Comment on the morphology of the erythrocytes.
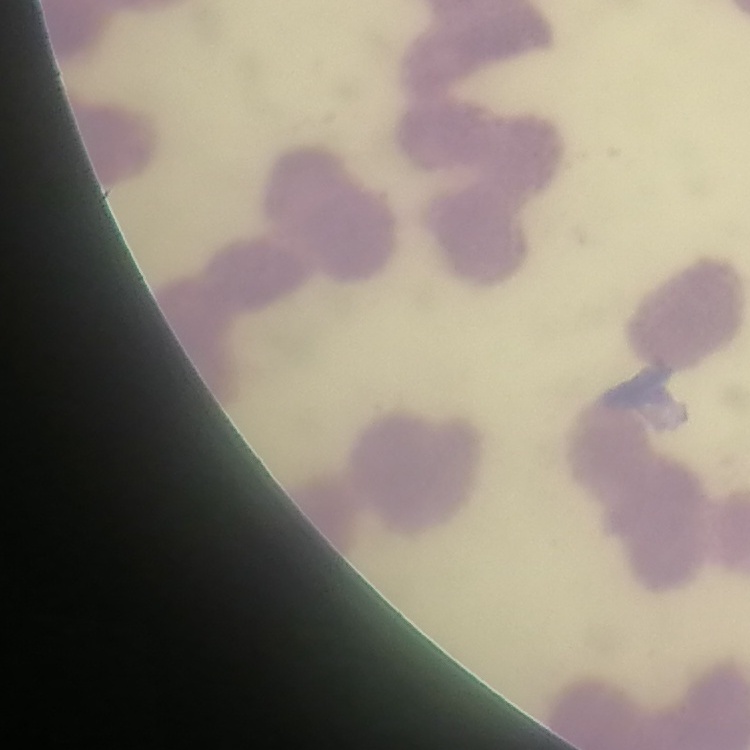
They show rouleaux formation.

image_type: square crop of a larger photomicrograph
preparation: thin blood smear
stain: Field's or Giemsa